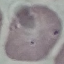
{
  "malaria_status": "uninfected",
  "preparation": "thin blood smear",
  "stain": "Giemsa",
  "capture": "smartphone through the microscope eyepiece",
  "image_type": "automatically extracted cell patch, resized to 64 × 64 pixels"
}